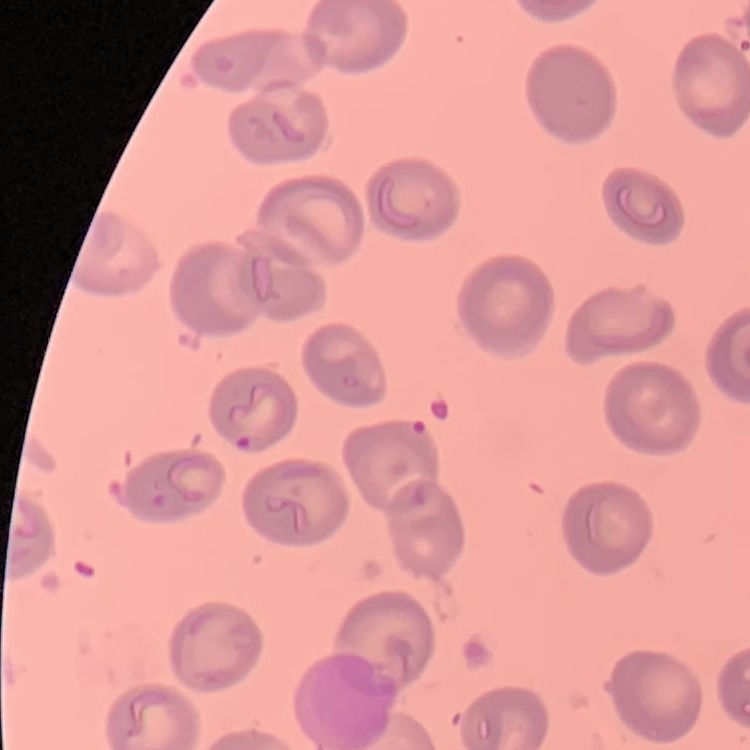

The erythrocytes exhibit no rouleaux formation. Square crop of a larger photomicrograph. Stained with either Field's or Giemsa. Thin blood film.